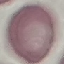
malaria status = uninfected
capture = smartphone camera at the microscope eyepiece
stain = Giemsa
image type = automatically extracted cell patch, resized to 64 × 64 pixels
preparation = thin blood film